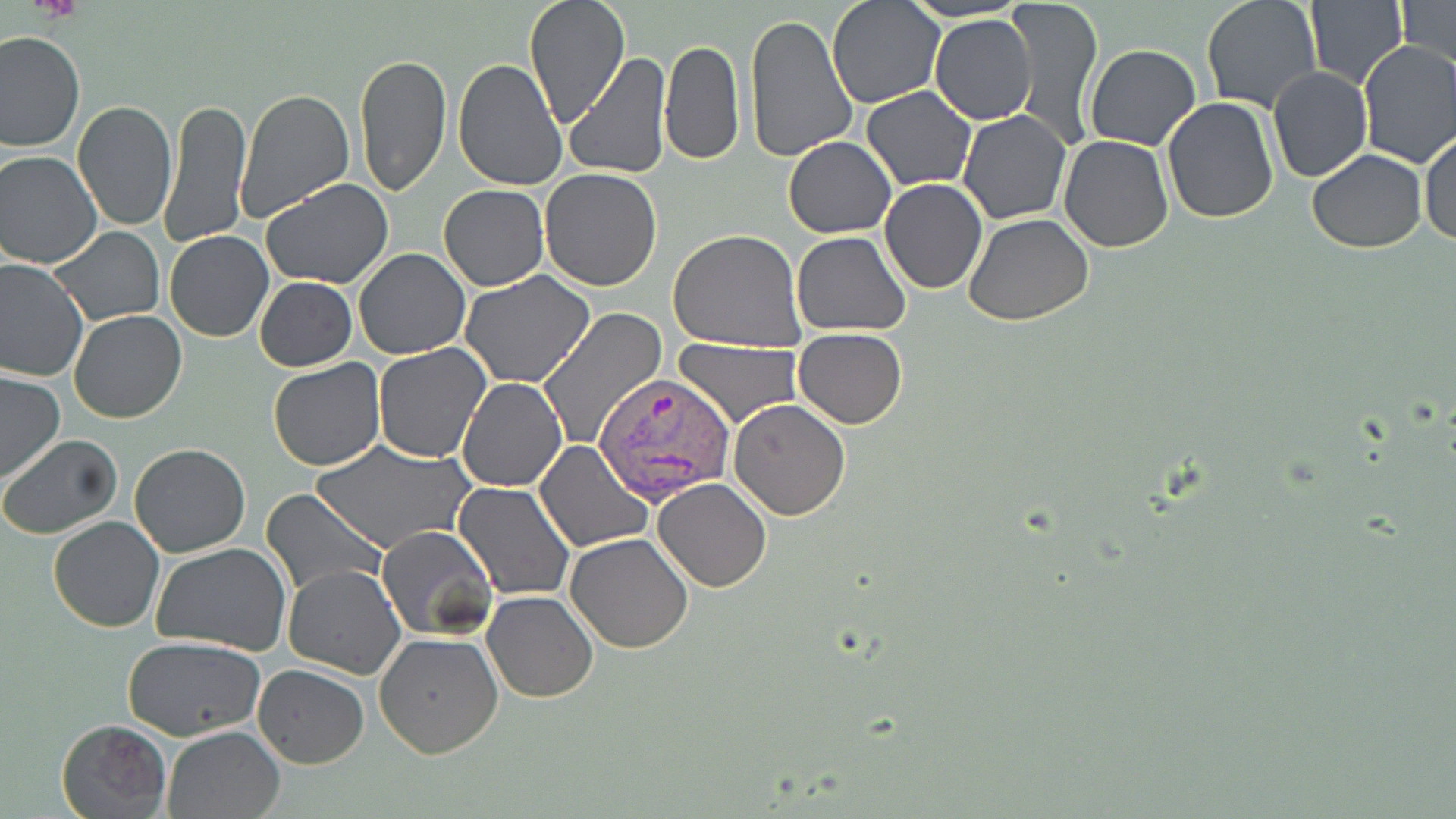
Summary:
  - Coordinate format: approximate bounding boxes as (x1, y1, x2, y2) in pixels
  - Uninfected red blood cell locations: (522, 0, 629, 125), (826, 0, 943, 108), (1007, 0, 1104, 148), (1200, 0, 1323, 114), (1304, 0, 1409, 90), (1394, 1, 1455, 70), (743, 12, 858, 163), (930, 13, 1037, 124), (1, 31, 83, 152), (660, 39, 744, 166), (1355, 40, 1456, 167), (1084, 43, 1202, 150), (354, 51, 452, 199), (566, 52, 669, 179), (452, 56, 566, 190), (1267, 66, 1372, 184), (235, 87, 355, 220), (861, 87, 976, 190), (1161, 96, 1282, 224), (160, 97, 252, 249), (71, 100, 177, 232), (958, 110, 1071, 225), (1419, 130, 1456, 247), (1059, 135, 1174, 254), (784, 136, 896, 238), (1307, 149, 1429, 252), (0, 150, 101, 268), (540, 168, 662, 291), (261, 178, 394, 288), (879, 178, 988, 293), (439, 184, 549, 291), (965, 214, 1095, 327), (48, 226, 164, 326), (667, 228, 807, 352), (164, 230, 273, 342), (791, 231, 911, 336), (353, 249, 470, 360), (0, 258, 89, 385), (460, 271, 596, 387), (254, 277, 357, 371), (2, 292, 139, 409), (537, 306, 668, 450), (68, 311, 187, 424), (793, 327, 907, 429), (674, 338, 802, 428), (371, 342, 491, 464), (266, 359, 385, 471), (0, 372, 66, 484), (458, 377, 567, 491), (728, 398, 852, 520), (0, 434, 124, 539), (536, 439, 652, 551), (313, 441, 473, 554), (130, 443, 251, 558), (652, 477, 772, 593), (454, 482, 575, 599), (259, 487, 385, 599), (46, 516, 165, 633), (377, 525, 496, 642), (565, 534, 694, 654), (151, 542, 294, 656), (285, 565, 404, 680), (481, 591, 598, 704), (374, 632, 503, 758), (123, 636, 266, 741), (254, 664, 368, 769), (56, 718, 172, 816), (162, 725, 285, 819)
  - Platelet locations: (31, 0, 83, 23)
  - Plasmodium vivax-infected red blood cell locations: (594, 373, 736, 506)
  - Slide-level diagnosis: Plasmodium vivax
  - Magnification: 1000x
  - Image size: 1456×819 pixels
  - Modality: light microscopy
  - Preparation: thin blood film
  - Field of view: single
  - Stain: May-Grünwald-Giemsa